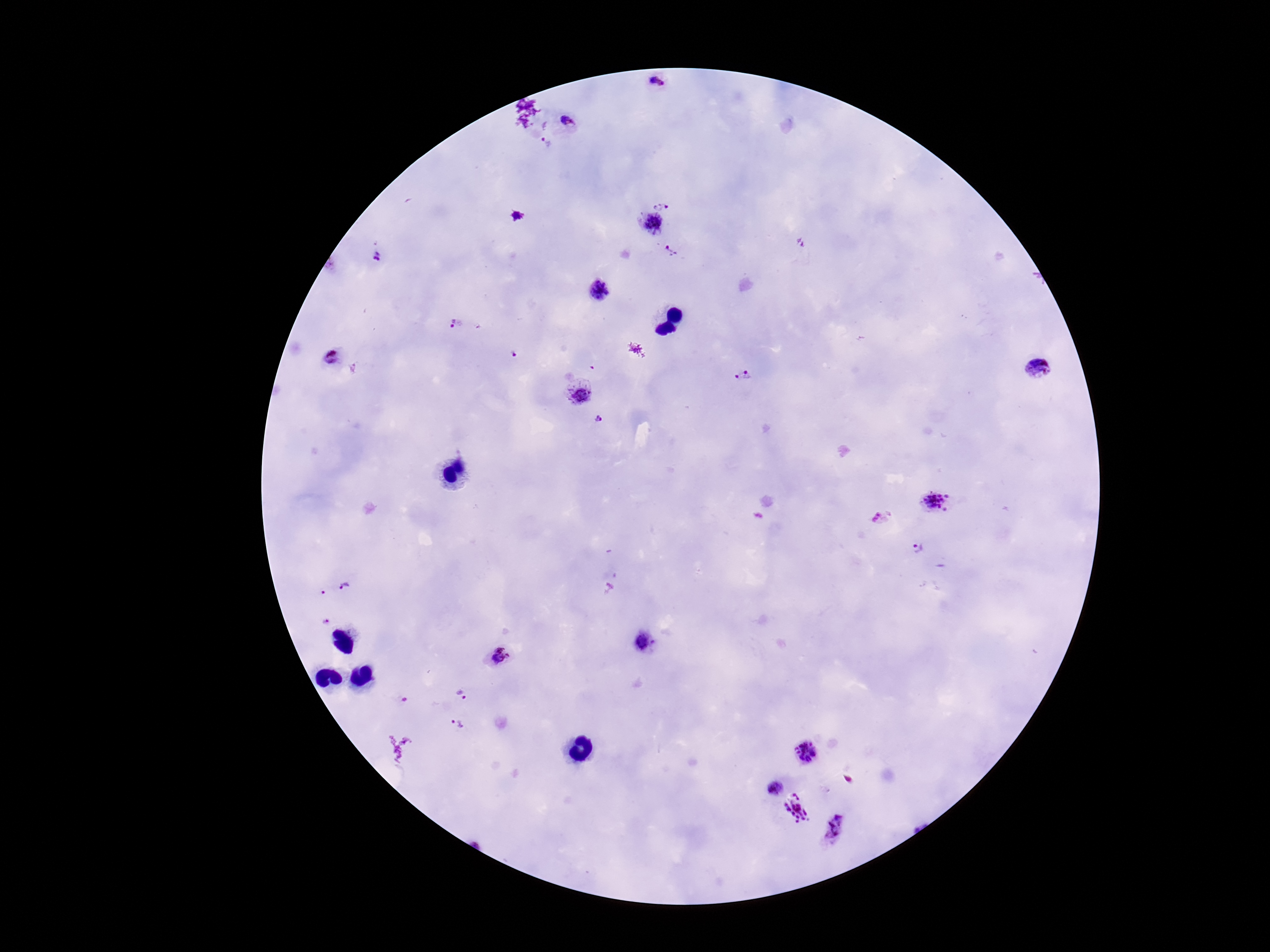
Approximate centers as [x, y] in pixels. Plasmodium parasite locations: [658, 83], [571, 120], [546, 143], [663, 204], [648, 225], [672, 252], [377, 259], [601, 290], [455, 325], [512, 355], [330, 359], [1038, 369], [742, 376], [580, 391], [598, 420], [935, 502], [916, 548], [347, 587], [324, 592], [325, 621], [642, 643], [498, 657], [463, 694], [455, 726], [806, 752], [773, 788], [797, 809], [834, 831]. Photographed through the microscope eyepiece with a smartphone camera. Thick blood smear. Giemsa stain. 100x magnification. Image is 1270×952 pixels. Single field of view. Patient malaria status: positive.